Give the extent of all uninfected red blood cells.
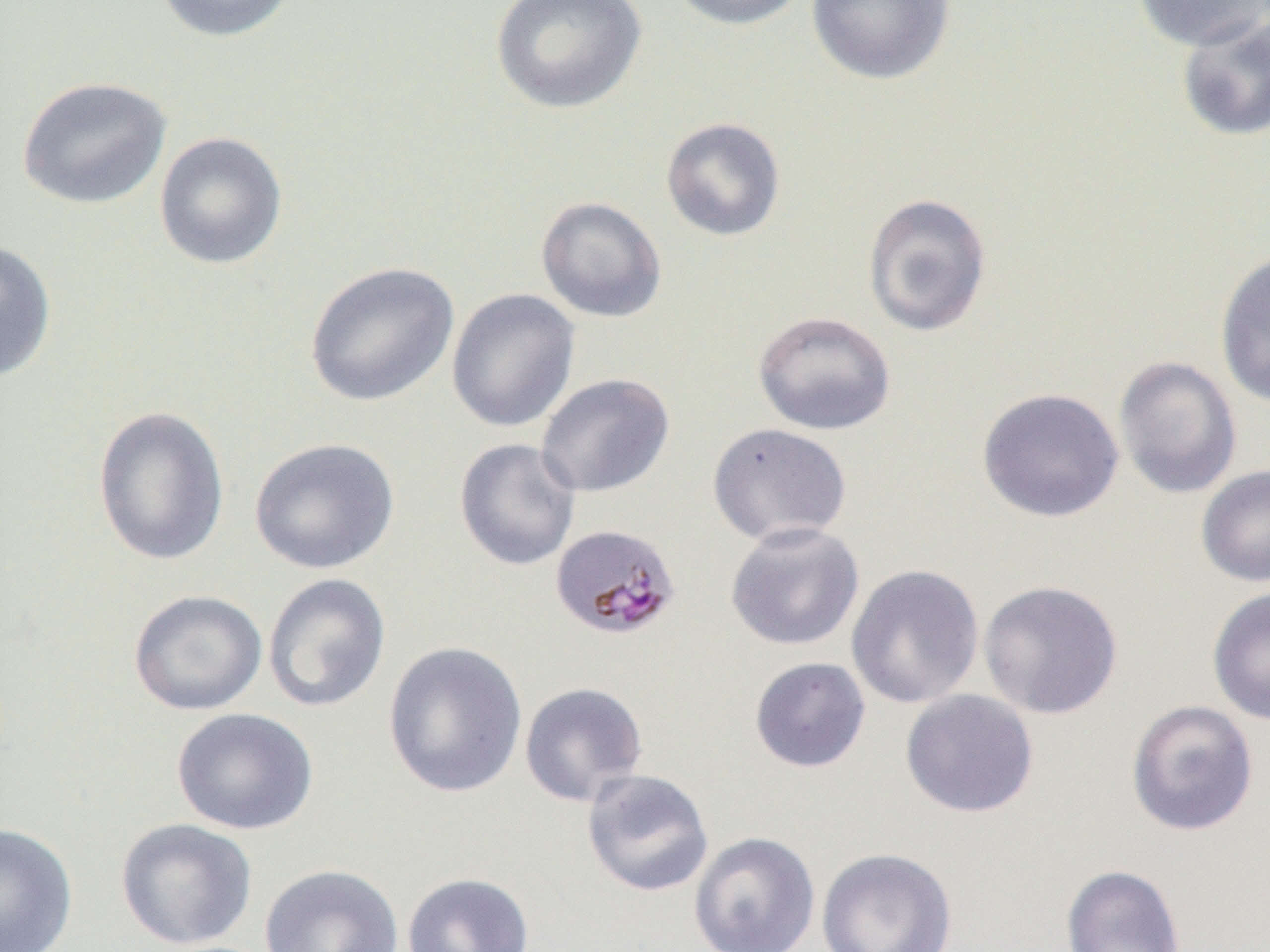
Approximate bounding boxes as [x1, y1, x2, y2] in pixels.
Uninfected red blood cells: [150, 0, 300, 43], [489, 0, 647, 114], [666, 0, 812, 31], [805, 0, 955, 86], [1134, 1, 1269, 52], [1175, 13, 1270, 143], [16, 76, 172, 210], [660, 117, 786, 241], [153, 131, 288, 270], [862, 192, 993, 337], [535, 196, 667, 323], [0, 238, 57, 383], [1214, 248, 1270, 410], [304, 261, 460, 407], [446, 288, 581, 433], [752, 310, 897, 436], [1113, 355, 1243, 499], [535, 372, 675, 498], [977, 387, 1124, 523], [91, 404, 230, 567], [707, 422, 853, 547], [249, 437, 400, 574], [454, 438, 582, 571], [1196, 464, 1270, 588], [725, 521, 865, 651], [846, 564, 984, 709], [262, 573, 391, 713], [978, 579, 1124, 719], [1207, 586, 1270, 725], [127, 589, 267, 716], [382, 640, 528, 798], [749, 656, 871, 773], [519, 681, 649, 807], [900, 689, 1039, 818], [1126, 700, 1260, 837], [171, 707, 318, 835], [581, 768, 714, 898], [115, 817, 258, 950], [0, 822, 79, 952], [688, 832, 820, 952], [816, 847, 957, 952], [259, 863, 404, 952], [1060, 863, 1186, 952], [401, 872, 535, 952].

Summary:
  - Plasmodium malariae-infected red blood cell locations: [550, 523, 681, 641]
  - Slide-level diagnosis: Plasmodium malariae
  - Image size: 1270×952 pixels
  - Magnification: 1000x
  - Modality: optical microscopy
  - Preparation: thin blood smear
  - Field of view: single